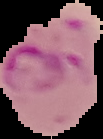
{
  "image_size": "103×139 pixels",
  "image_type": "segmented cell region on a black background",
  "preparation": "thin blood smear",
  "result": "Plasmodium parasites detected"
}